Locate every Plasmodium parasite.
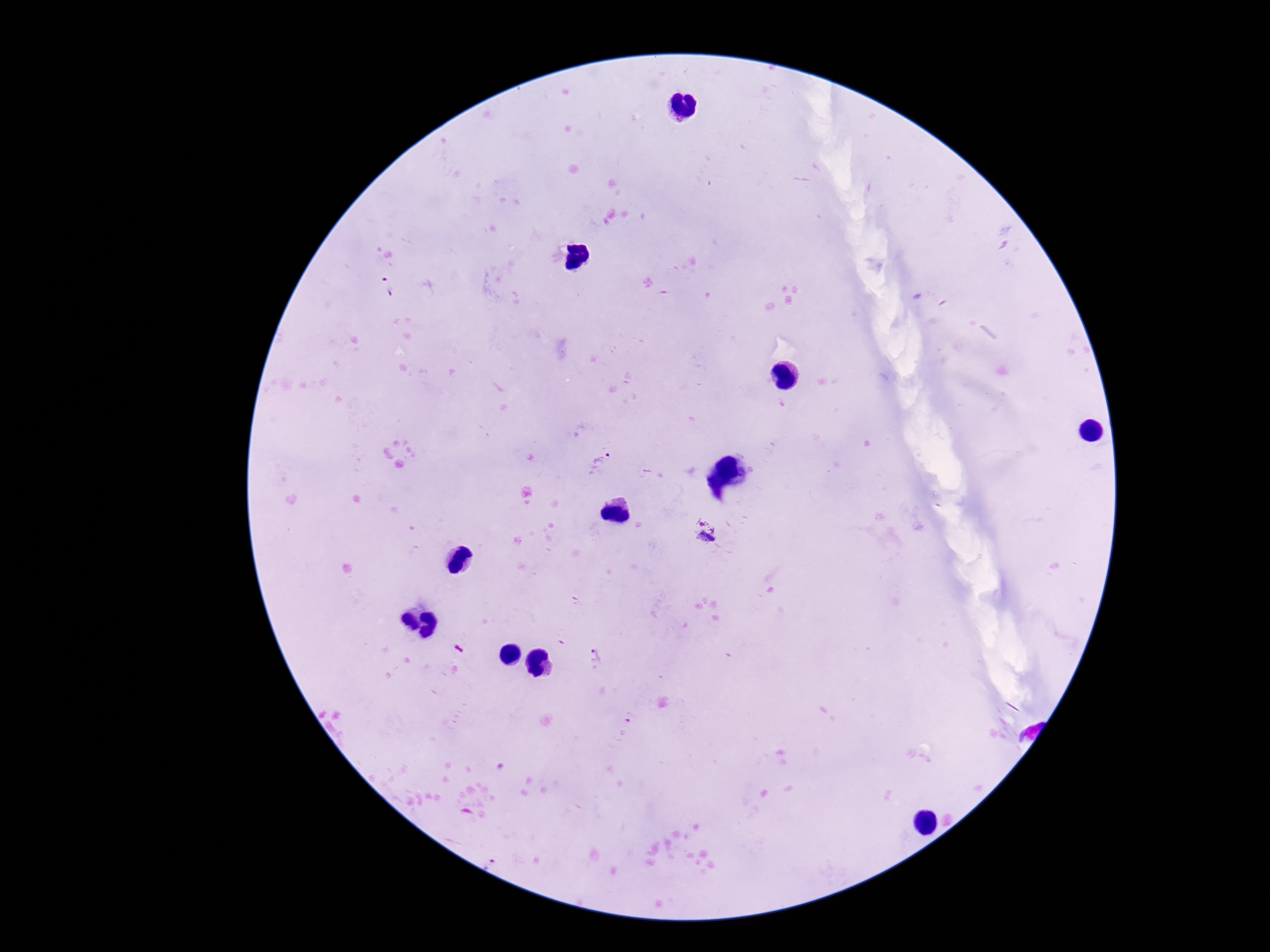

Approximate centers as [x, y] in pixels.
Plasmodium parasites: [388, 287], [601, 461], [705, 533], [596, 655].

preparation = thick peripheral-blood smear
field of view = single
patient malaria status = positive
magnification = 100x
stain = Giemsa
image size = 1270×952 pixels
capture = smartphone camera through the microscope eyepiece